State which parasite is depicted.
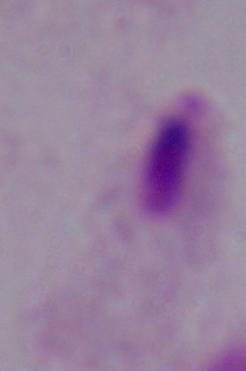

This is a trichomonad.

Captured at 1000x magnification. Micrograph.